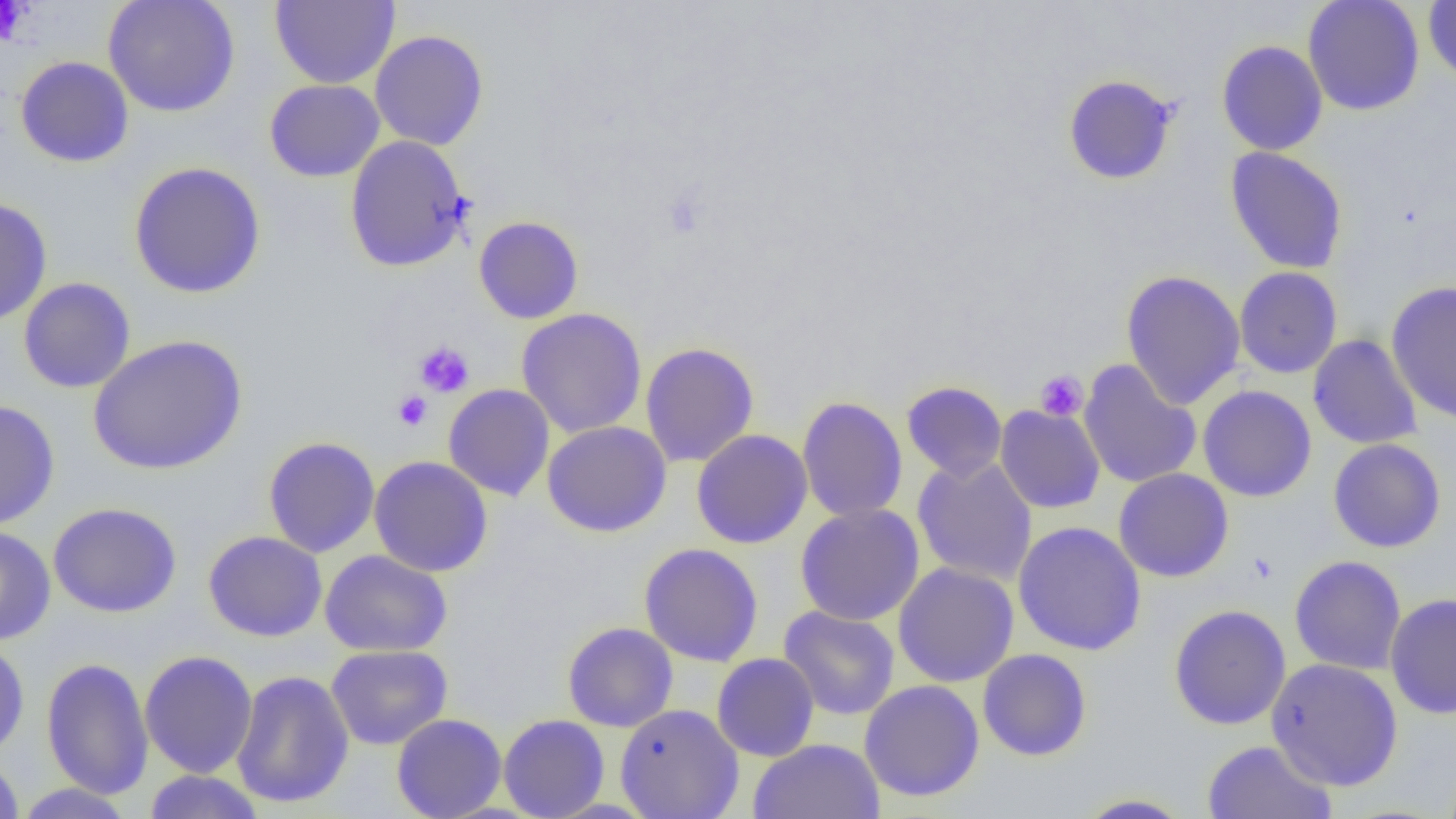
{
  "slide_level_diagnosis": "no evidence of blood parasites",
  "platelet_locations": "approximate bounding boxes as (x1,y1)-(x2,y2) corner pairs in pixels: (0,1)-(30,46), (414,342)-(475,397), (1035,370)-(1088,421), (393,390)-(432,431)",
  "magnification": "1000x",
  "modality": "light microscopy",
  "uninfected_red_blood_cell_locations": "approximate bounding boxes as (x1,y1)-(x2,y2) corner pairs in pixels: (103,0)-(240,117), (270,0)-(400,89), (1303,0)-(1425,116), (1423,1)-(1456,84), (370,30)-(489,151), (1216,40)-(1328,156), (15,56)-(134,168), (1062,74)-(1179,185), (264,79)-(385,182), (344,135)-(471,272), (1225,147)-(1348,274), (129,161)-(266,299), (0,196)-(52,327), (473,216)-(584,324), (1234,267)-(1342,378), (1120,269)-(1246,410), (18,277)-(135,394), (1386,281)-(1456,423), (516,307)-(647,438), (88,334)-(247,475), (1308,334)-(1423,449), (640,341)-(759,468), (1078,359)-(1201,489), (901,381)-(1007,481), (443,384)-(555,501), (1197,385)-(1317,502), (797,396)-(908,522), (0,400)-(60,529), (995,405)-(1105,513), (542,421)-(672,537), (692,430)-(812,549), (263,437)-(380,558), (1328,438)-(1446,553), (369,456)-(493,577), (912,456)-(1037,586), (1113,468)-(1234,583), (48,502)-(182,617), (794,503)-(925,626), (1013,521)-(1147,655), (0,526)-(56,645), (203,530)-(328,642), (639,543)-(764,666), (320,549)-(453,657), (1289,555)-(1407,675), (892,562)-(1019,687), (1385,592)-(1456,719), (1168,604)-(1292,730), (779,605)-(900,720), (562,621)-(678,732), (0,638)-(29,760), (326,645)-(452,749), (977,648)-(1092,761), (139,650)-(257,778), (711,653)-(820,762), (41,657)-(154,799), (1265,658)-(1404,791), (231,670)-(355,809), (859,679)-(985,802), (614,703)-(744,819), (391,713)-(507,819), (498,714)-(610,819), (748,738)-(885,819), (1202,740)-(1338,819), (0,752)-(24,818), (142,770)-(266,818), (13,783)-(135,818), (1073,793)-(1196,818)",
  "field_of_view": "single",
  "image_size": "1456×819 pixels",
  "preparation": "thin blood film"
}